Report the malaria status of this cell.
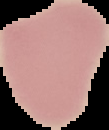

It is uninfected.

preparation = thin blood smear
image size = 109×130 pixels
image type = cell region segmented out of the field of view; surrounding area masked to black